Locate every blood parasite and identify its species.
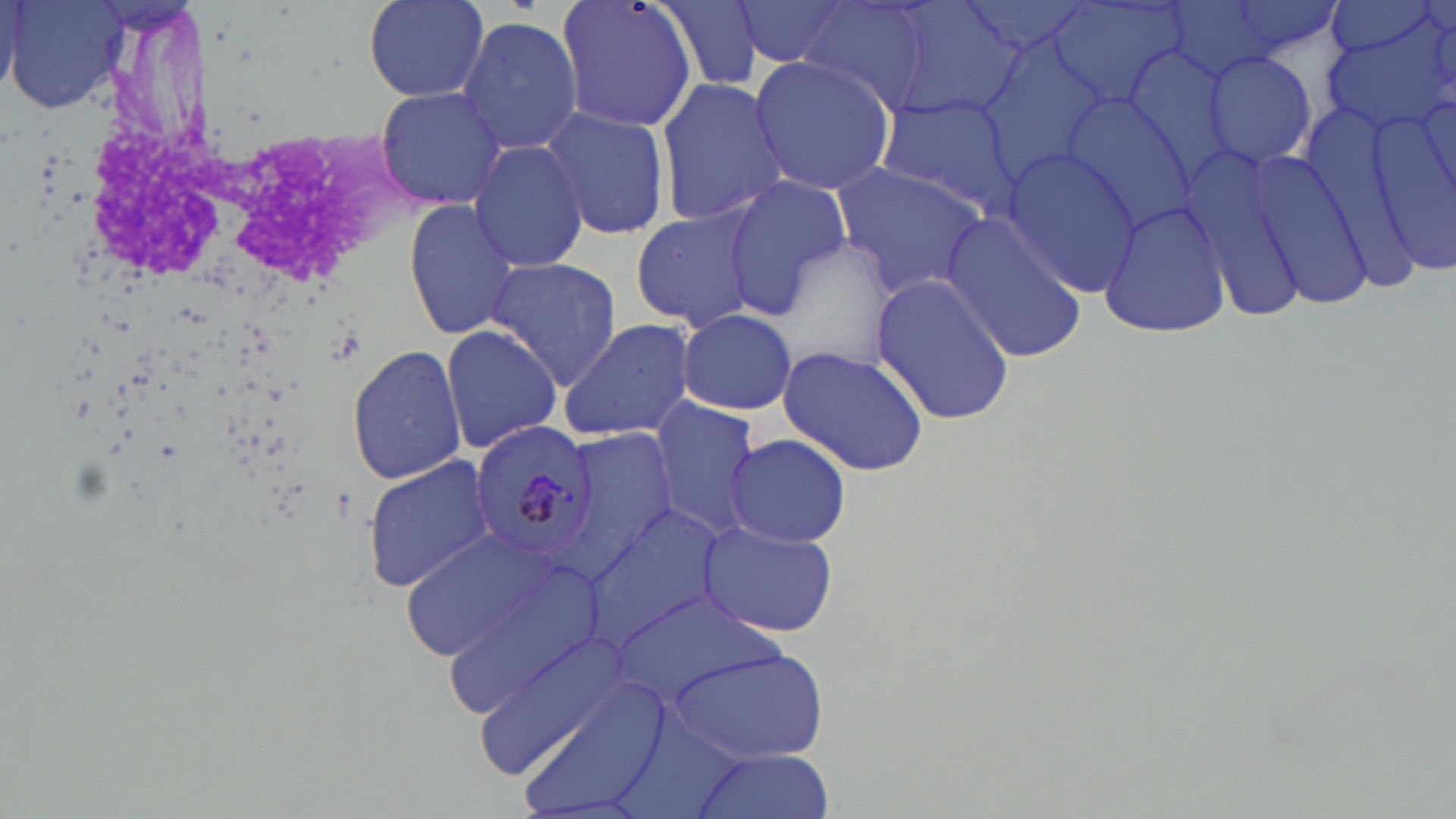
Approximate bounding boxes as (x1, y1, x2, y2) in pixels.
Plasmodium malariae-infected red blood cells: (470, 420, 603, 570).
No Plasmodium falciparum, Plasmodium ovale, Plasmodium vivax, Babesia divergens, or Trypanosoma brucei observed.

Summary:
  - Uninfected red blood cell locations: (4, 0, 129, 117), (360, 0, 490, 101), (554, 0, 700, 134), (655, 0, 767, 93), (730, 0, 853, 69), (877, 0, 1026, 123), (957, 0, 1101, 59), (1218, 0, 1349, 63), (1325, 0, 1439, 60), (796, 1, 937, 111), (1047, 2, 1188, 111), (0, 3, 20, 96), (1320, 12, 1456, 137), (457, 15, 584, 155), (975, 31, 1110, 179), (1115, 41, 1240, 188), (1201, 51, 1318, 171), (748, 53, 898, 197), (655, 77, 789, 225), (375, 87, 508, 209), (872, 93, 1022, 216), (1055, 96, 1200, 231), (1360, 97, 1456, 275), (540, 105, 669, 242), (467, 139, 590, 274), (999, 147, 1143, 294), (1176, 150, 1315, 323), (1249, 155, 1380, 312), (831, 159, 995, 297), (721, 175, 849, 318), (1097, 198, 1234, 340), (405, 202, 521, 340), (629, 206, 763, 332), (938, 214, 1088, 362), (484, 258, 623, 392), (869, 270, 1017, 425), (676, 308, 797, 415), (556, 317, 697, 442), (440, 324, 562, 455), (776, 343, 930, 476), (347, 344, 468, 485), (649, 396, 765, 541), (560, 428, 680, 568), (726, 433, 852, 548), (362, 456, 497, 595), (583, 504, 733, 653), (698, 520, 838, 638), (401, 530, 558, 664), (420, 542, 613, 716), (476, 629, 628, 779), (671, 647, 827, 763), (513, 677, 669, 817), (688, 747, 835, 819)
  - Slide-level diagnosis: Plasmodium malariae
  - Stain: May-Grünwald-Giemsa
  - Preparation: thin blood film
  - Magnification: 1000x
  - Image size: 1456×819 pixels
  - Field of view: single
  - Modality: light microscopy